Report the malaria status of this cell.
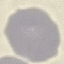

It is uninfected.

stain = Giemsa
preparation = thin blood film
capture = smartphone camera at the microscope eyepiece
image type = cell patch, automatically extracted from a larger field of view and resized to 64 × 64 pixels